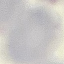
malaria status = uninfected
capture = smartphone camera at the microscope eyepiece
preparation = thin blood film
image type = automatically extracted cell patch, resized to 64 × 64 pixels
stain = Giemsa